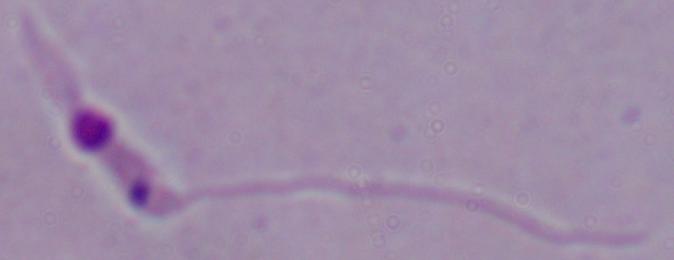
magnification = 1000x
modality = micrograph
identification = Leishmania